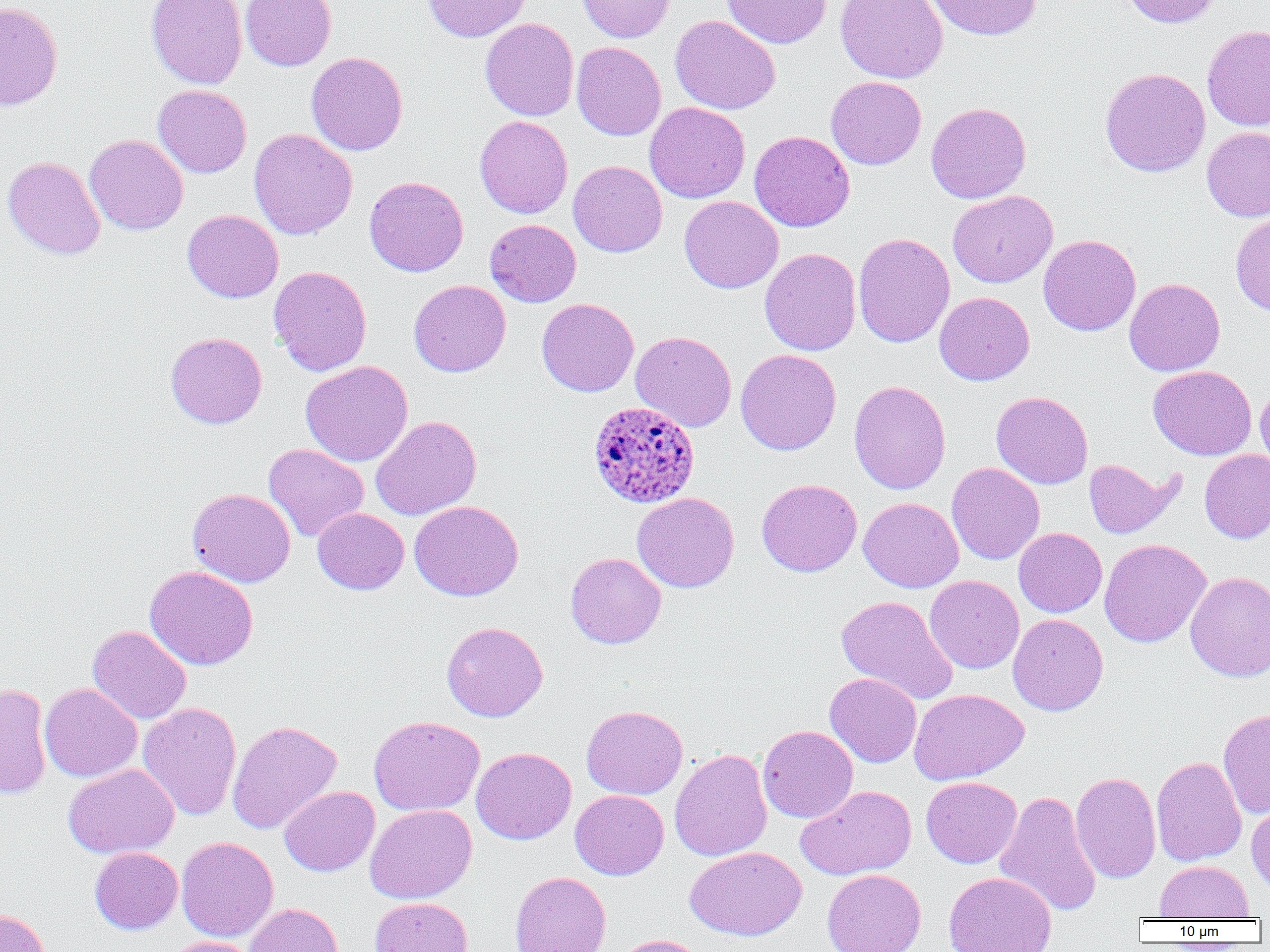

slide-level diagnosis = Plasmodium ovale
modality = light microscopy
field of view = single
magnification = 1000x
Plasmodium ovale-infected red blood cell locations = approximate bounding boxes as (x1, y1, x2, y2) in pixels: (587, 401, 699, 509)
uninfected red blood cell locations = approximate bounding boxes as (x1, y1, x2, y2) in pixels: (146, 0, 247, 89), (240, 0, 336, 71), (423, 0, 530, 42), (575, 0, 675, 43), (721, 0, 831, 48), (835, 0, 948, 83), (928, 0, 1042, 41), (1120, 0, 1220, 28), (0, 2, 63, 111), (670, 15, 781, 115), (480, 18, 579, 121), (1202, 25, 1270, 131), (572, 42, 665, 141), (306, 52, 408, 156), (1099, 68, 1211, 177), (826, 76, 926, 170), (153, 84, 252, 178), (644, 102, 750, 203), (926, 102, 1031, 203), (474, 115, 573, 218), (1202, 127, 1270, 221), (249, 128, 357, 240), (749, 130, 855, 232), (84, 134, 188, 235), (3, 156, 105, 259), (568, 160, 667, 257), (364, 176, 468, 277), (947, 190, 1058, 288), (679, 195, 783, 294), (182, 209, 284, 303), (1231, 211, 1270, 316), (485, 219, 581, 307), (852, 233, 955, 348), (1038, 234, 1141, 336), (760, 248, 861, 356), (268, 266, 373, 376), (1124, 278, 1225, 376), (408, 279, 511, 377), (934, 292, 1034, 385), (537, 298, 639, 397), (631, 331, 737, 431), (165, 332, 267, 428), (735, 349, 841, 456), (300, 360, 413, 466), (1148, 365, 1257, 460), (849, 380, 950, 494), (1255, 380, 1270, 474), (991, 391, 1093, 489), (371, 416, 482, 520), (263, 443, 369, 542), (1200, 449, 1270, 543), (1083, 459, 1182, 539), (947, 462, 1044, 565), (756, 478, 862, 577), (187, 488, 295, 587), (631, 492, 739, 592), (858, 497, 964, 592), (409, 500, 524, 601), (312, 507, 409, 594), (1013, 527, 1106, 617), (1099, 539, 1211, 648), (565, 552, 666, 649), (145, 565, 259, 670), (1185, 571, 1270, 682), (925, 575, 1024, 674), (836, 595, 958, 705), (1007, 614, 1108, 716), (441, 621, 548, 722), (87, 625, 192, 724), (824, 673, 921, 768), (39, 682, 142, 782), (0, 683, 52, 799), (909, 689, 1029, 784), (138, 702, 242, 820), (582, 705, 687, 799), (1218, 707, 1270, 818), (369, 715, 485, 816), (227, 720, 342, 833), (757, 725, 858, 823), (471, 746, 576, 845), (670, 749, 772, 862), (1151, 756, 1247, 866), (63, 764, 179, 858), (1070, 771, 1161, 883), (921, 776, 1022, 868), (796, 785, 917, 880), (279, 786, 379, 876), (570, 790, 669, 880), (994, 790, 1101, 917), (1246, 795, 1270, 894), (364, 804, 477, 904), (176, 837, 278, 942), (684, 846, 806, 941), (89, 847, 183, 934), (1155, 860, 1253, 920), (821, 869, 926, 952), (943, 871, 1057, 952), (509, 872, 611, 952), (370, 897, 473, 952), (244, 902, 344, 952), (0, 907, 50, 952), (613, 934, 707, 952), (159, 936, 259, 952)
preparation = thin blood smear
image size = 1270×952 pixels